Identify the parasite.
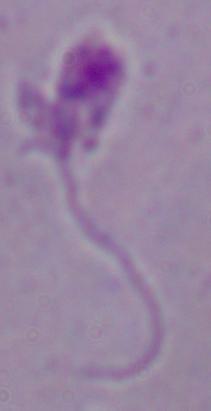

Leishmania.

magnification = 1000x
modality = micrograph